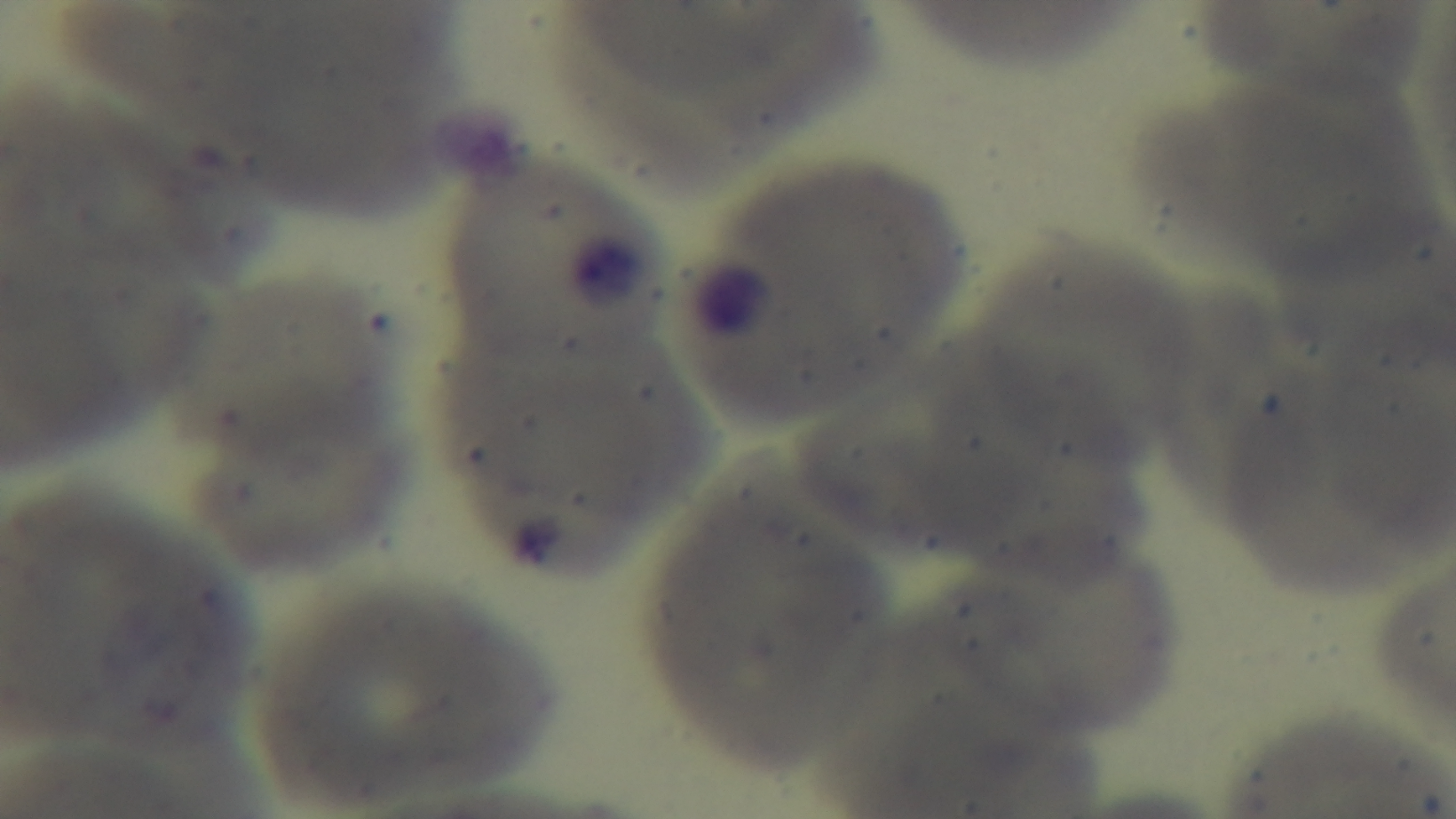

Giemsa stain. Mounted 4K digital camera. Malaria status: uninfected. Preparation: thin. One field from the slide. Oil-immersion objective, 100x. Photomicrograph.